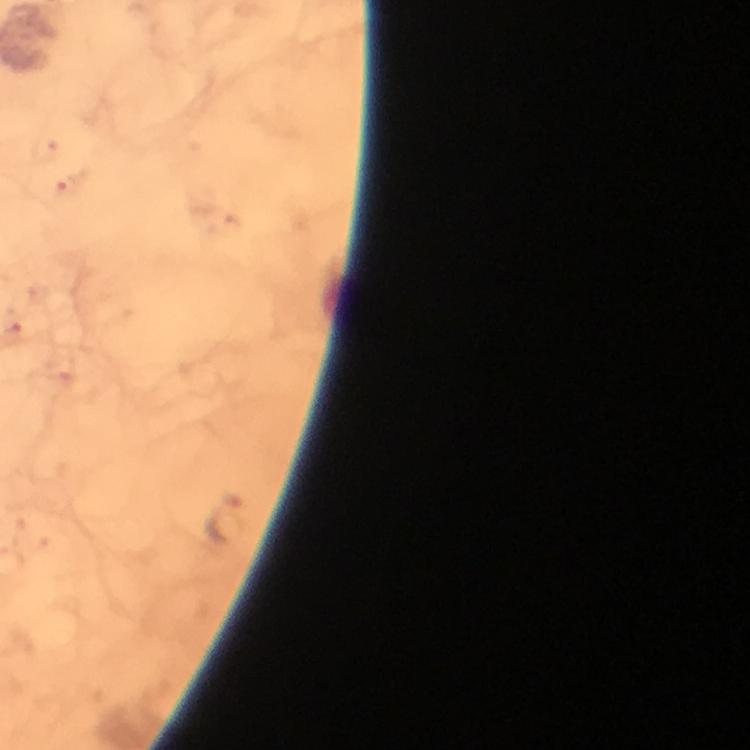 Approximate centers as (x, y) in pixels. Plasmodium parasite locations: (64, 188), (227, 519). From a diagnostic examination for malaria. Giemsa-stained preparation. 100x magnification. Immersion oil applied. Thick smear. A crop from one field of view. Image is 750×750 pixels. Photographed with a smartphone mounted on the microscope.